Identify the parasite.
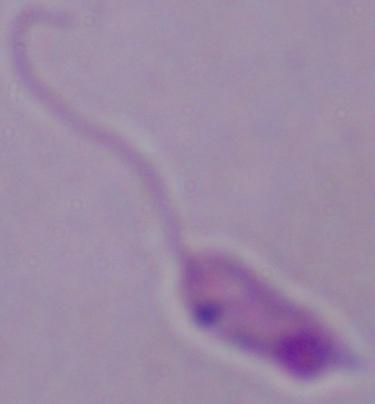

This is Leishmania.

Photomicrograph. 1000x magnification.